State which parasite is depicted.
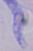
This is a trypanosome.

{
  "magnification": "1000x",
  "modality": "photomicrograph"
}